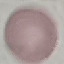
result: negative for malaria parasites
image_type: cell patch, automatically extracted from a larger field of view and resized to 64 × 64 pixels
capture: smartphone through the microscope eyepiece
stain: Giemsa
preparation: thin blood film